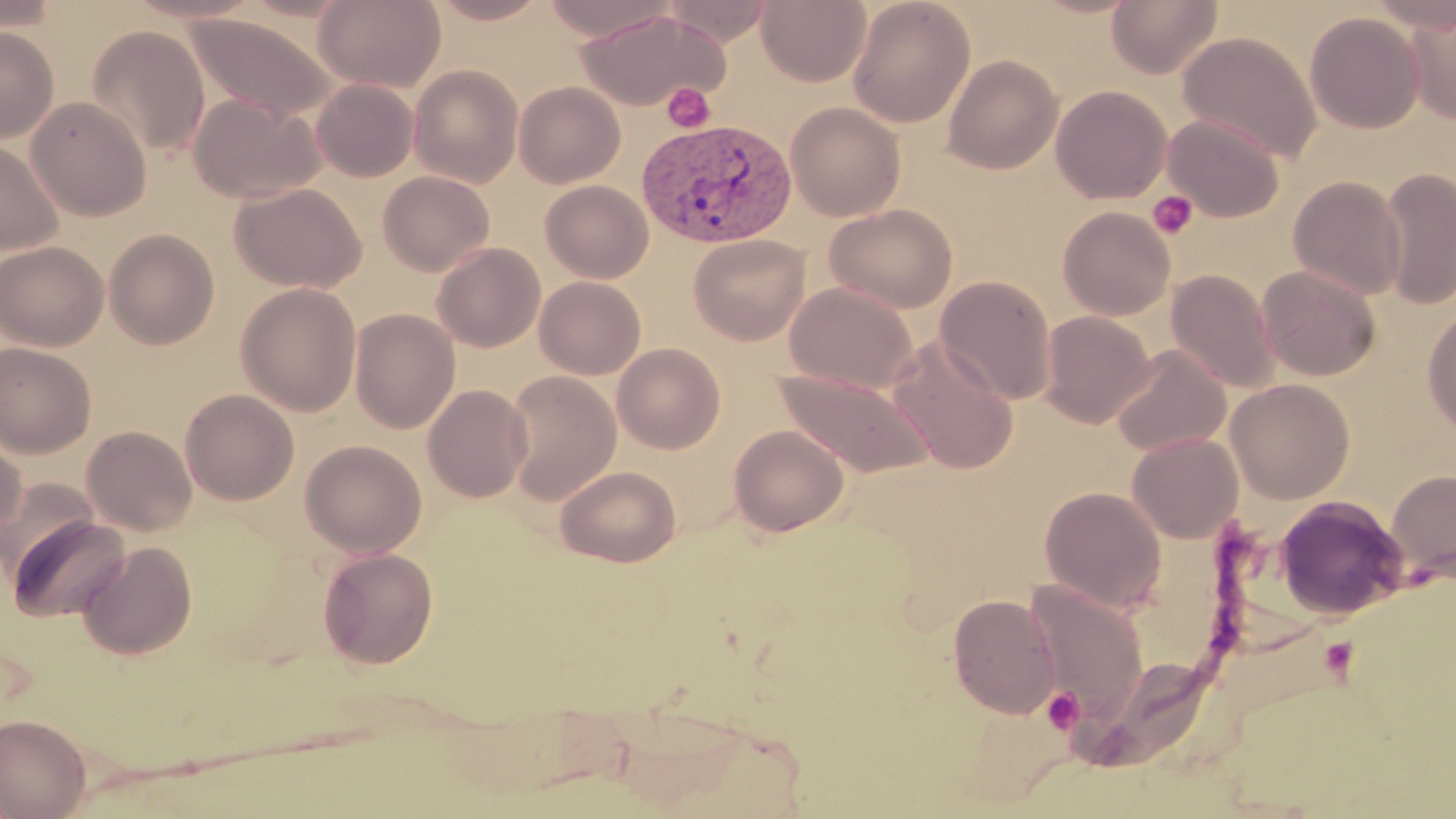
Summary:
  - Coordinate format: approximate bounding boxes as named x1/y1/x2/y2 corners in pixels
  - Platelet locations: (x1=662, y1=82, x2=716, y2=133), (x1=1147, y1=190, x2=1199, y2=240), (x1=1319, y1=637, x2=1359, y2=679), (x1=1042, y1=688, x2=1085, y2=734)
  - Uninfected red blood cell locations: (x1=0, y1=0, x2=61, y2=34), (x1=122, y1=0, x2=266, y2=24), (x1=314, y1=0, x2=446, y2=92), (x1=427, y1=0, x2=552, y2=24), (x1=541, y1=0, x2=679, y2=42), (x1=756, y1=0, x2=871, y2=86), (x1=847, y1=0, x2=975, y2=127), (x1=1106, y1=0, x2=1223, y2=78), (x1=663, y1=1, x2=779, y2=46), (x1=1404, y1=6, x2=1456, y2=125), (x1=576, y1=9, x2=729, y2=110), (x1=1304, y1=11, x2=1425, y2=134), (x1=185, y1=12, x2=339, y2=123), (x1=86, y1=25, x2=210, y2=157), (x1=0, y1=27, x2=59, y2=143), (x1=1177, y1=31, x2=1323, y2=163), (x1=943, y1=54, x2=1063, y2=174), (x1=409, y1=64, x2=524, y2=187), (x1=310, y1=78, x2=418, y2=182), (x1=514, y1=81, x2=626, y2=188), (x1=1051, y1=85, x2=1172, y2=204), (x1=189, y1=93, x2=326, y2=204), (x1=26, y1=96, x2=151, y2=221), (x1=785, y1=101, x2=906, y2=221), (x1=1162, y1=114, x2=1285, y2=221), (x1=0, y1=138, x2=64, y2=257), (x1=1379, y1=168, x2=1456, y2=309), (x1=377, y1=170, x2=495, y2=276), (x1=1288, y1=176, x2=1407, y2=299), (x1=540, y1=179, x2=654, y2=283), (x1=230, y1=182, x2=367, y2=292), (x1=823, y1=203, x2=958, y2=313), (x1=1057, y1=206, x2=1175, y2=320), (x1=104, y1=228, x2=220, y2=349), (x1=688, y1=234, x2=810, y2=345), (x1=0, y1=240, x2=109, y2=351), (x1=431, y1=242, x2=546, y2=352), (x1=1257, y1=265, x2=1381, y2=381), (x1=1166, y1=269, x2=1280, y2=393), (x1=534, y1=276, x2=646, y2=380), (x1=935, y1=276, x2=1056, y2=404), (x1=235, y1=282, x2=361, y2=416), (x1=784, y1=282, x2=919, y2=395), (x1=1422, y1=304, x2=1456, y2=437), (x1=350, y1=308, x2=461, y2=434), (x1=1040, y1=310, x2=1156, y2=428), (x1=887, y1=334, x2=1020, y2=475), (x1=0, y1=342, x2=97, y2=459), (x1=612, y1=343, x2=725, y2=453), (x1=1111, y1=346, x2=1231, y2=456), (x1=775, y1=368, x2=935, y2=478), (x1=504, y1=371, x2=622, y2=504), (x1=1225, y1=378, x2=1355, y2=503), (x1=422, y1=384, x2=533, y2=503), (x1=180, y1=389, x2=299, y2=505), (x1=729, y1=424, x2=849, y2=537), (x1=82, y1=425, x2=197, y2=536), (x1=0, y1=434, x2=26, y2=543), (x1=1127, y1=434, x2=1244, y2=544), (x1=300, y1=439, x2=427, y2=558), (x1=555, y1=465, x2=681, y2=566), (x1=1386, y1=469, x2=1456, y2=583), (x1=1, y1=478, x2=99, y2=579), (x1=1039, y1=486, x2=1167, y2=613), (x1=1274, y1=496, x2=1409, y2=621), (x1=5, y1=515, x2=131, y2=623), (x1=77, y1=540, x2=197, y2=660), (x1=317, y1=546, x2=439, y2=668), (x1=1022, y1=581, x2=1150, y2=725), (x1=948, y1=593, x2=1061, y2=718), (x1=1068, y1=658, x2=1217, y2=769), (x1=0, y1=713, x2=92, y2=818)
  - Plasmodium vivax-infected red blood cell locations: (x1=636, y1=116, x2=798, y2=249)
  - Slide-level diagnosis: Plasmodium vivax
  - Field of view: one of a larger specimen
  - Modality: optical microscopy
  - Preparation: thin blood film
  - Magnification: 1000x
  - Image size: 1456×819 pixels
  - Stain: May-Grünwald-Giemsa